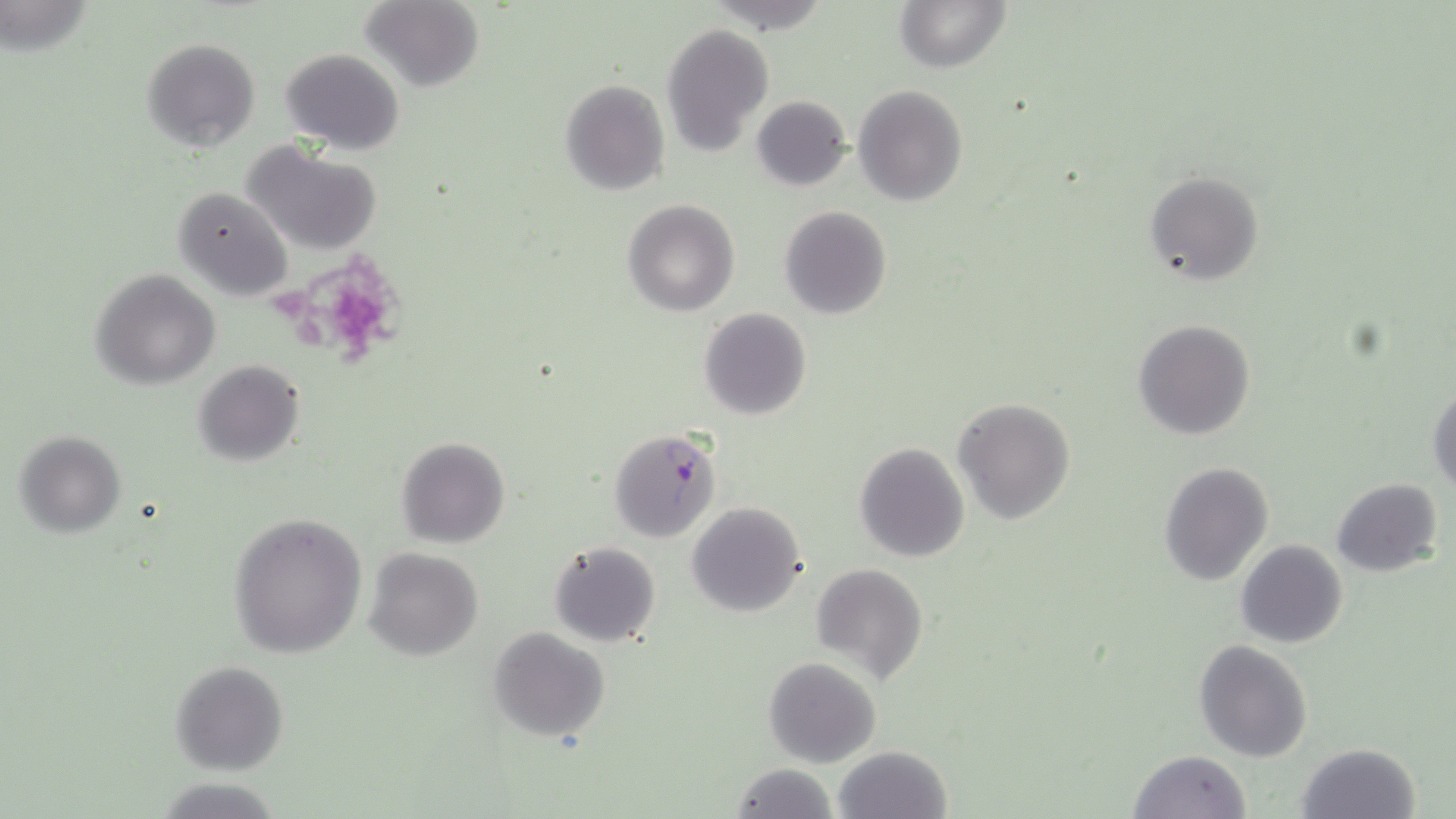
Summary:
  - Coordinate format: approximate bounding boxes as (x1, y1, x2, y2) in pixels
  - Plasmodium falciparum-infected red blood cell locations: (611, 427, 723, 541)
  - Uninfected red blood cell locations: (361, 0, 483, 91), (894, 0, 1011, 74), (661, 23, 774, 157), (142, 37, 260, 152), (281, 48, 405, 154), (560, 79, 669, 197), (853, 84, 967, 206), (752, 95, 852, 191), (244, 141, 382, 256), (1144, 171, 1263, 284), (174, 186, 293, 302), (622, 200, 739, 316), (778, 205, 893, 320), (90, 269, 220, 388), (698, 307, 812, 420), (1133, 318, 1256, 440), (193, 359, 305, 468), (1428, 383, 1456, 493), (953, 397, 1075, 524), (14, 430, 126, 537), (396, 436, 510, 549), (855, 442, 969, 562), (1159, 461, 1273, 586), (1331, 478, 1443, 577), (687, 501, 808, 617), (229, 510, 367, 658), (1235, 539, 1349, 648), (548, 540, 662, 647), (364, 548, 484, 660), (811, 562, 927, 681), (488, 629, 610, 743), (1195, 640, 1312, 761), (764, 657, 882, 767), (170, 660, 289, 773), (1295, 742, 1421, 819), (833, 746, 952, 819), (1126, 750, 1252, 819), (729, 763, 836, 819)
  - Slide-level diagnosis: Plasmodium falciparum
  - Modality: optical microscopy
  - Stain: May-Grünwald-Giemsa
  - Preparation: thin blood film
  - Image size: 1456×819 pixels
  - Field of view: single
  - Magnification: 1000x